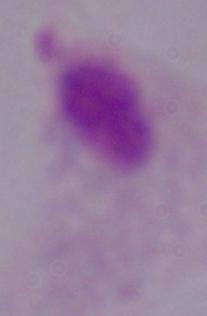

Summary:
  - Identification: trichomonad
  - Magnification: 1000x
  - Modality: micrograph